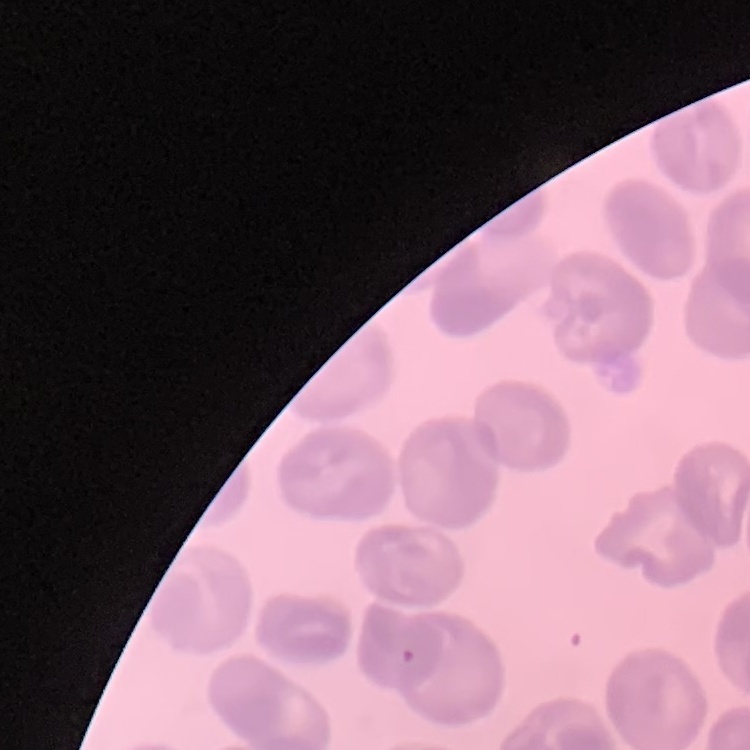

Summary:
  - Erythrocyte morphology: no rouleaux formation
  - Preparation: thin peripheral smear
  - Stain: Field's or Giemsa
  - Image type: square crop of a larger photomicrograph